Outline platelets.
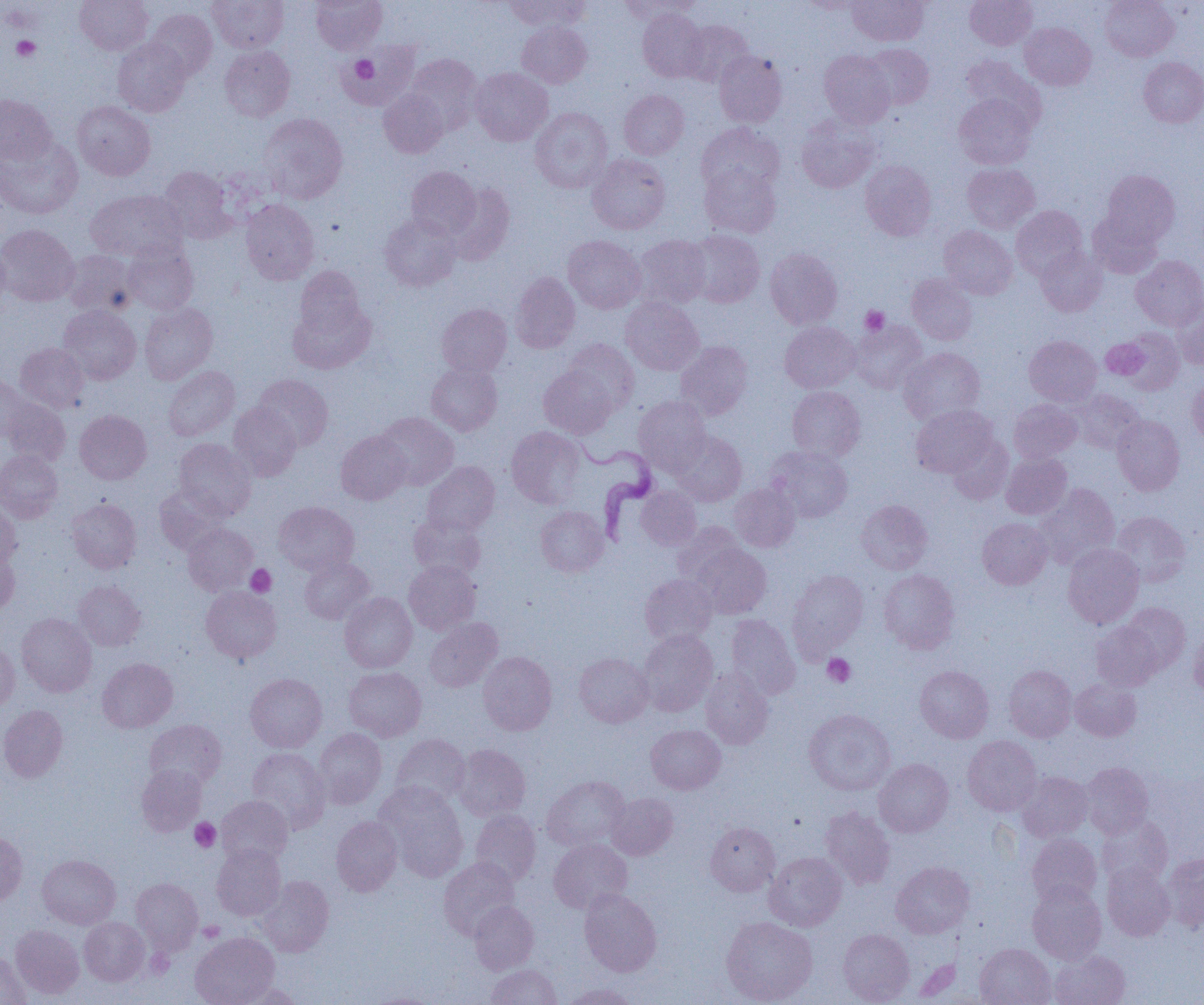

Approximate bounding boxes as (x1, y1, x2, y2) in pixels.
Platelets: (11, 36, 40, 61), (349, 55, 379, 84), (860, 306, 890, 335), (1101, 337, 1150, 378), (246, 564, 276, 597), (822, 653, 856, 687), (190, 818, 220, 851), (198, 921, 225, 942).

Summary:
  - Trypanosoma brucei locations: (567, 432, 660, 543)
  - Uninfected red blood cell locations: (75, 0, 152, 55), (207, 0, 288, 52), (311, 0, 387, 54), (504, 0, 589, 31), (620, 0, 702, 23), (848, 0, 929, 46), (965, 0, 1037, 50), (1100, 0, 1178, 61), (798, 1, 870, 13), (146, 8, 217, 80), (637, 9, 708, 82), (681, 20, 753, 87), (517, 22, 591, 88), (1020, 23, 1095, 90), (113, 37, 191, 117), (344, 41, 419, 109), (863, 43, 934, 109), (219, 45, 296, 121), (819, 50, 896, 128), (713, 51, 786, 127), (406, 54, 482, 132), (961, 56, 1044, 128), (1139, 57, 1204, 127), (471, 67, 553, 145), (379, 89, 448, 158), (619, 90, 688, 159), (954, 93, 1037, 169), (0, 94, 56, 165), (72, 101, 155, 181), (530, 107, 612, 193), (259, 113, 348, 203), (795, 117, 878, 194), (697, 122, 784, 197), (0, 136, 83, 218), (587, 153, 671, 234), (860, 160, 936, 240), (962, 163, 1040, 233), (700, 165, 780, 238), (159, 166, 236, 243), (406, 166, 481, 239), (1102, 170, 1179, 245), (445, 183, 515, 264), (85, 189, 187, 263), (241, 199, 319, 285), (1011, 205, 1087, 279), (1088, 211, 1163, 278), (380, 212, 461, 291), (0, 224, 79, 307), (939, 225, 1017, 299), (686, 230, 764, 308), (563, 235, 646, 313), (633, 235, 711, 309), (0, 238, 10, 311), (122, 245, 198, 315), (1036, 247, 1107, 316), (765, 248, 842, 329), (63, 250, 138, 316), (1131, 255, 1204, 329), (295, 266, 364, 337), (510, 272, 580, 353), (906, 273, 977, 345), (620, 297, 703, 375), (1172, 297, 1204, 370), (288, 298, 376, 374), (139, 303, 217, 384), (437, 304, 512, 377), (58, 305, 141, 384), (850, 321, 927, 393), (780, 322, 859, 393), (1117, 328, 1184, 395), (1024, 335, 1102, 406), (1101, 338, 1149, 379), (564, 339, 639, 412), (675, 341, 753, 420), (15, 342, 89, 412), (900, 347, 984, 424), (426, 361, 502, 435), (164, 366, 239, 440), (539, 366, 617, 438), (0, 374, 33, 442), (253, 374, 333, 450), (1187, 375, 1204, 444), (787, 386, 865, 460), (1068, 389, 1146, 454), (633, 395, 711, 473), (1, 398, 70, 466), (1009, 399, 1081, 463), (228, 403, 301, 481), (911, 405, 997, 478), (75, 410, 151, 484), (375, 412, 459, 490), (1112, 415, 1185, 495), (506, 426, 586, 509), (336, 430, 411, 504), (671, 431, 747, 506), (946, 434, 1013, 504), (173, 438, 256, 520), (767, 446, 854, 522), (0, 449, 63, 523), (1001, 452, 1072, 519), (422, 461, 500, 535), (729, 483, 801, 552), (1033, 483, 1119, 569), (154, 485, 228, 556), (635, 486, 701, 550), (67, 498, 141, 573), (856, 499, 932, 574), (0, 501, 21, 567), (274, 501, 359, 575), (535, 506, 609, 576), (1112, 511, 1191, 586), (408, 515, 486, 581), (977, 517, 1051, 589), (672, 522, 745, 585), (183, 523, 258, 595), (690, 543, 771, 618), (1062, 543, 1144, 628), (0, 547, 20, 615), (299, 556, 375, 624), (404, 561, 481, 634), (879, 569, 959, 653), (787, 570, 869, 657), (639, 573, 717, 646), (73, 581, 145, 651), (201, 586, 281, 663), (340, 592, 417, 672), (1121, 603, 1191, 673), (17, 612, 96, 697), (726, 614, 801, 699), (424, 618, 502, 692), (1091, 621, 1163, 691), (1189, 628, 1204, 699), (638, 630, 717, 715), (0, 641, 19, 711), (478, 651, 557, 735), (574, 653, 654, 728), (97, 658, 178, 733), (915, 665, 993, 743), (1004, 665, 1076, 742), (344, 667, 426, 741), (700, 668, 773, 749), (245, 673, 326, 752), (1070, 677, 1141, 741), (0, 705, 67, 782), (804, 708, 895, 795), (144, 719, 227, 790), (646, 724, 725, 794), (314, 728, 387, 808), (390, 734, 470, 808), (963, 736, 1042, 816), (452, 744, 530, 820), (247, 747, 330, 832), (874, 758, 953, 837), (1080, 762, 1154, 838), (136, 764, 207, 836), (1016, 771, 1092, 841), (542, 775, 630, 852), (375, 782, 468, 880), (606, 792, 678, 859), (216, 795, 293, 866), (820, 806, 895, 890), (470, 809, 541, 886), (1097, 815, 1173, 887), (331, 816, 402, 896), (705, 821, 780, 895), (0, 832, 27, 905), (1027, 833, 1102, 906), (548, 839, 632, 913), (212, 843, 286, 920), (764, 852, 846, 931), (1161, 853, 1204, 931), (37, 854, 120, 929), (438, 857, 520, 939), (891, 861, 974, 938), (1102, 862, 1174, 941), (258, 876, 334, 956), (131, 878, 202, 953), (1028, 882, 1107, 964), (579, 888, 661, 976), (469, 901, 538, 974), (721, 916, 817, 1005), (79, 917, 149, 985), (11, 925, 84, 999), (838, 928, 914, 1004), (190, 932, 279, 1005), (975, 943, 1055, 1005), (1049, 950, 1130, 1005), (0, 951, 31, 1005), (486, 964, 561, 1005), (235, 983, 302, 1005), (562, 983, 639, 1005), (371, 993, 437, 1004)
  - Slide-level diagnosis: Trypanosoma brucei
  - Image size: 1204×1005 pixels
  - Field of view: one of a larger specimen
  - Magnification: 1000x
  - Preparation: thin blood film
  - Modality: light microscopy